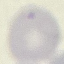
Result: no malaria parasites seen. Giemsa-stained preparation. Photographed with a smartphone camera at the microscope eyepiece. Thin blood smear. Cell patch, automatically extracted from a larger field of view and resized to 64 × 64 pixels.